Assess this cell for malaria.
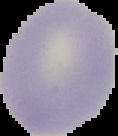

Uninfected.

Summary:
  - Image size: 118×136 pixels
  - Image type: segmented cell region on a black background
  - Preparation: thin blood film